Assess this cell for malaria.
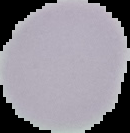

It is uninfected.

From a thin blood film. Image is 130×133 pixels. The area outside the segmented cell region is set to black.